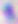

identification: Toxoplasma gondii
modality: photomicrograph
magnification: 400x